Assess the morphology of the erythrocytes.
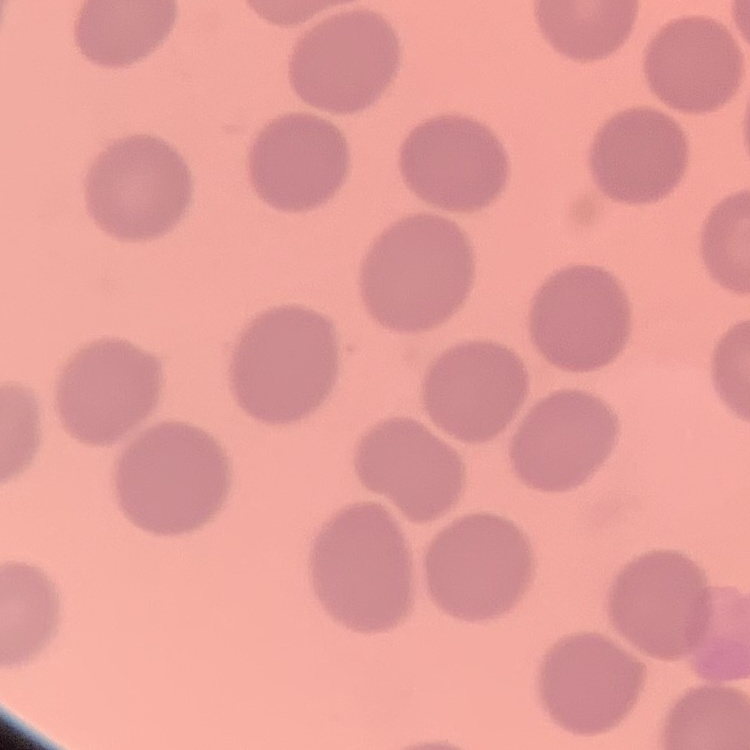

No rouleaux formation.

Summary:
  - Preparation: thin peripheral smear
  - Image type: one tile cut from a larger photomicrograph
  - Stain: Field's or Giemsa